Outline each blood parasite and name the species.
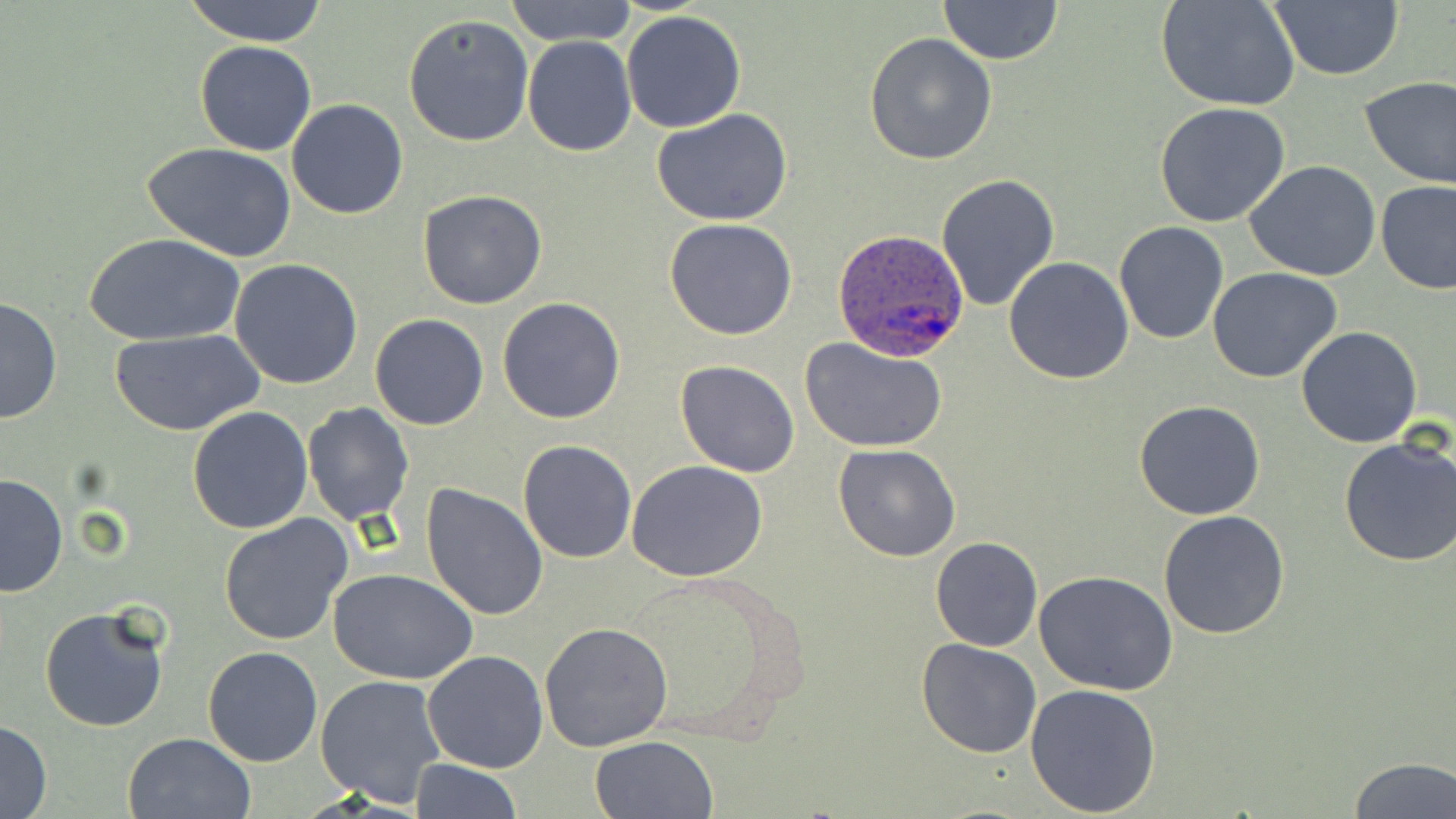

Approximate bounding boxes as named x1/y1/x2/y2 corners in pixels.
Plasmodium ovale-infected red blood cells: (x1=833, y1=229, x2=970, y2=362).
No Plasmodium falciparum, Plasmodium malariae, Plasmodium vivax, Babesia divergens, or Trypanosoma brucei observed.

Uninfected red blood cell locations: (x1=183, y1=0, x2=329, y2=46), (x1=938, y1=0, x2=1062, y2=65), (x1=1157, y1=0, x2=1301, y2=113), (x1=1268, y1=0, x2=1405, y2=82), (x1=502, y1=1, x2=640, y2=46), (x1=622, y1=10, x2=747, y2=133), (x1=402, y1=12, x2=534, y2=147), (x1=517, y1=25, x2=741, y2=146), (x1=864, y1=33, x2=998, y2=165), (x1=521, y1=36, x2=636, y2=157), (x1=195, y1=39, x2=316, y2=156), (x1=1360, y1=74, x2=1456, y2=191), (x1=286, y1=99, x2=411, y2=219), (x1=1156, y1=101, x2=1291, y2=228), (x1=651, y1=109, x2=793, y2=227), (x1=142, y1=141, x2=297, y2=263), (x1=1243, y1=161, x2=1383, y2=282), (x1=937, y1=173, x2=1060, y2=311), (x1=1375, y1=181, x2=1456, y2=295), (x1=417, y1=190, x2=548, y2=310), (x1=664, y1=218, x2=798, y2=340), (x1=1114, y1=222, x2=1229, y2=345), (x1=83, y1=234, x2=241, y2=347), (x1=1005, y1=257, x2=1134, y2=385), (x1=229, y1=259, x2=362, y2=390), (x1=1207, y1=267, x2=1345, y2=384), (x1=497, y1=297, x2=626, y2=425), (x1=0, y1=298, x2=60, y2=426), (x1=369, y1=313, x2=489, y2=431), (x1=1295, y1=326, x2=1422, y2=447), (x1=112, y1=328, x2=265, y2=437), (x1=799, y1=338, x2=948, y2=452), (x1=675, y1=361, x2=800, y2=477), (x1=1133, y1=401, x2=1266, y2=520), (x1=301, y1=403, x2=415, y2=525), (x1=186, y1=406, x2=314, y2=535), (x1=1338, y1=436, x2=1456, y2=568), (x1=517, y1=439, x2=637, y2=563), (x1=833, y1=444, x2=961, y2=562), (x1=626, y1=460, x2=770, y2=582), (x1=0, y1=474, x2=69, y2=598), (x1=421, y1=483, x2=549, y2=619), (x1=1158, y1=511, x2=1290, y2=640), (x1=218, y1=514, x2=354, y2=648), (x1=930, y1=537, x2=1042, y2=652), (x1=618, y1=566, x2=808, y2=738), (x1=328, y1=567, x2=479, y2=684), (x1=1034, y1=570, x2=1178, y2=695), (x1=39, y1=606, x2=170, y2=733), (x1=539, y1=623, x2=673, y2=750), (x1=915, y1=638, x2=1042, y2=758), (x1=203, y1=647, x2=324, y2=767), (x1=423, y1=649, x2=548, y2=773), (x1=315, y1=673, x2=448, y2=807), (x1=1026, y1=681, x2=1162, y2=817), (x1=0, y1=719, x2=51, y2=818), (x1=122, y1=731, x2=256, y2=818), (x1=590, y1=736, x2=718, y2=819), (x1=1348, y1=756, x2=1455, y2=819), (x1=410, y1=758, x2=522, y2=817). Slide-level diagnosis: Plasmodium ovale. Image is 1456×819 pixels. Thin blood smear. May-Grünwald-Giemsa-stained preparation. 1000x magnification. Single field of view. Light microscopy.